Give the position of every leukocyte visible.
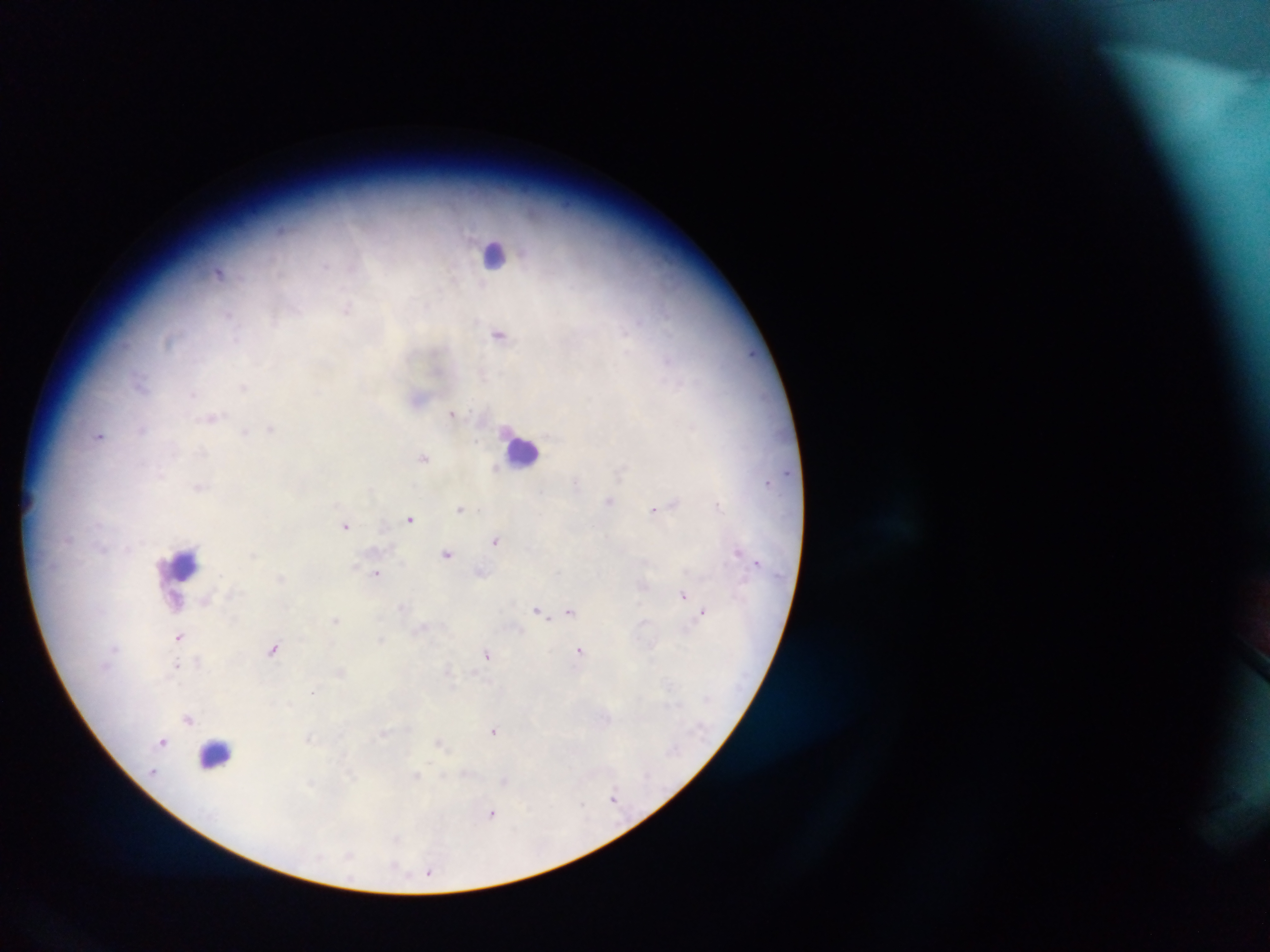

Approximate centers as {x, y} in pixels.
Leukocytes: {494, 257}, {524, 451}, {184, 563}, {217, 754}.
One object is labeled both Plasmodium parasite and leukocyte by the source: {176, 600}.

field_of_view: single
preparation: thick blood film
country: Ghana
image_size: 1270×952 pixels
plasmodium_parasite_locations: 'approximate centers as {x, y} in pixels: {281, 229}, {325, 266}, {219, 272}, {348, 307}, {229, 315}, {499, 334}, {167, 342}, {667, 359}, {140, 381}, {243, 387}, {316, 391}, {192, 393}, {453, 413}, {213, 418}, {142, 429}, {271, 429}, {245, 433}, {100, 436}, {477, 441}, {424, 458}, {495, 468}, {160, 474}, {576, 483}, {199, 487}, {609, 501}, {675, 503}, {717, 505}, {460, 508}, {653, 510}, {410, 519}, {346, 525}, {496, 541}, {737, 551}, {253, 554}, {447, 554}, {757, 561}, {482, 572}, {377, 573}, {683, 595}, {205, 602}, {403, 607}, {538, 610}, {569, 611}, {703, 612}, {335, 620}, {421, 628}, {179, 636}, {381, 639}, {273, 649}, {579, 650}, {488, 654}, {198, 661}, {176, 665}, {448, 670}, {340, 671}, {314, 691}, {188, 719}, {494, 731}, {382, 734}, {308, 738}, {164, 741}, {440, 742}, {152, 773}, {351, 775}, {416, 775}, {310, 784}, {613, 797}, {581, 805}, {492, 814}, {396, 838}, {349, 855}, {396, 868}, {429, 871}'
capture: mobile-phone photograph through a microscope